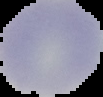 The area outside the segmented cell region is set to black. From a thin blood smear. Image is 103×97 pixels. Result: negative for malaria parasites.